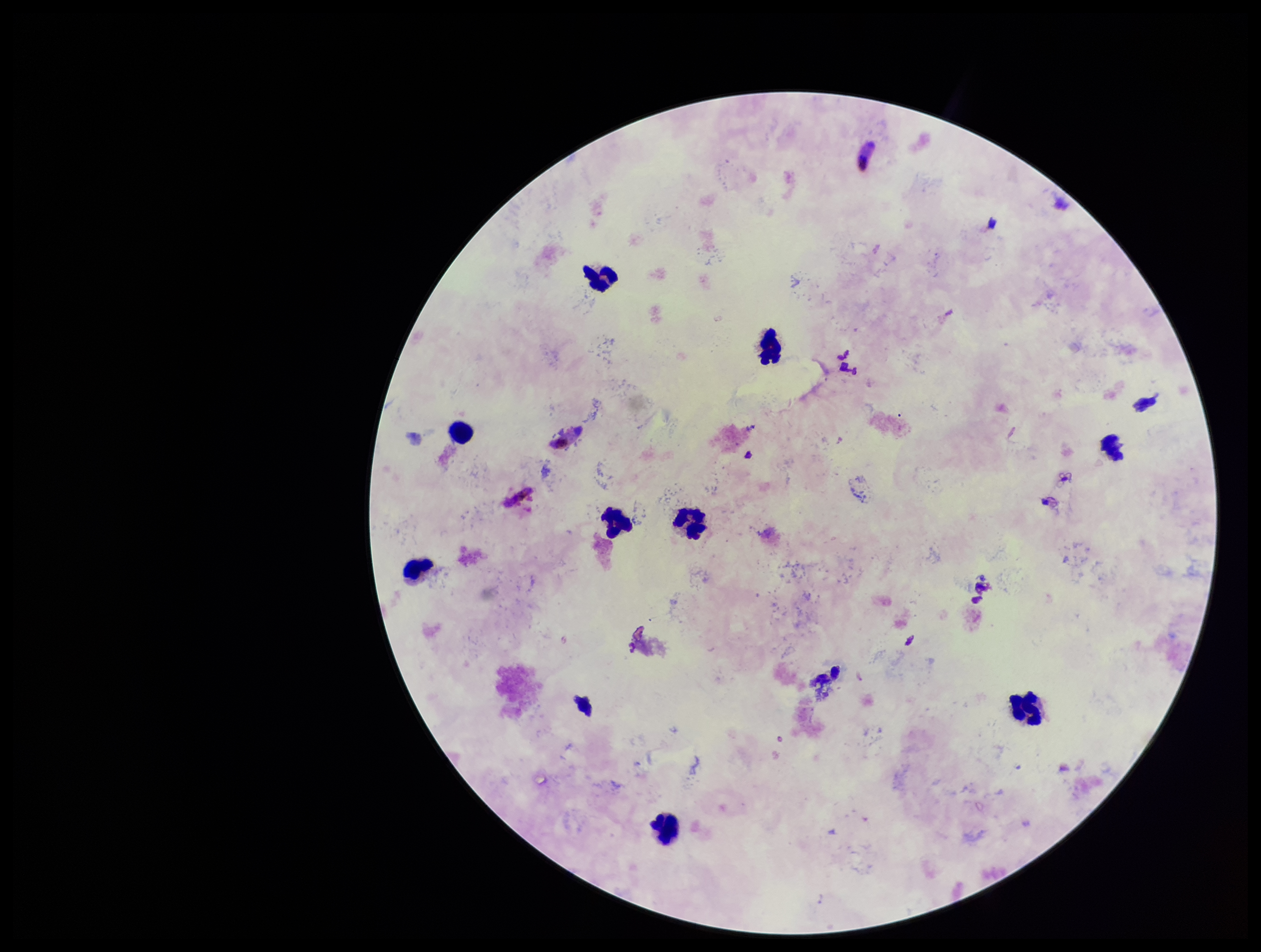

capture: smartphone photograph through the microscope eyepiece
stain: Giemsa
patient_malaria_status: positive
field_of_view: single
parasite_count: 0
species_reported_for_this_patient: Plasmodium falciparum
leukocyte_count: 9
image_size: 1261×952 pixels
preparation: thick smear
plasmodium_parasites: none seen